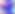
magnification = 400x
identification = Toxoplasma gondii
modality = photomicrograph